Outline each blood parasite and name the species.
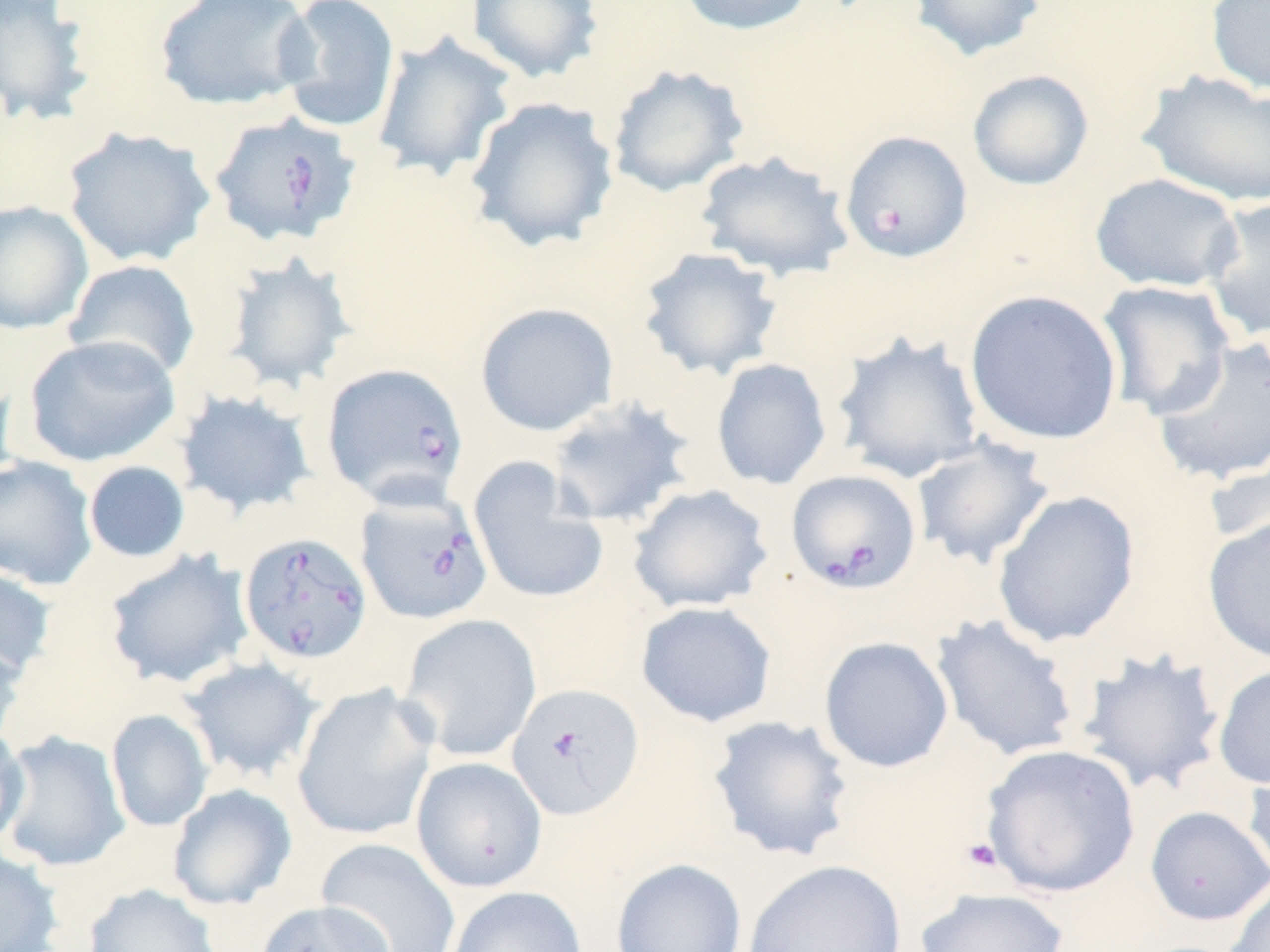
Approximate bounding boxes as (x1, y1, x2, y2) in pixels.
Babesia divergens-infected red blood cells: (206, 111, 362, 248), (321, 362, 469, 508), (785, 468, 922, 594), (355, 489, 493, 625), (238, 531, 373, 664), (506, 683, 644, 821).
No Plasmodium falciparum, Plasmodium ovale, Plasmodium malariae, Plasmodium vivax, or Trypanosoma brucei observed.

Uninfected red blood cell locations: (153, 0, 316, 112), (274, 0, 401, 134), (465, 0, 604, 84), (675, 0, 818, 36), (907, 0, 1047, 62), (1205, 0, 1270, 96), (0, 1, 97, 128), (371, 30, 518, 183), (606, 64, 749, 198), (966, 69, 1094, 191), (1137, 69, 1270, 207), (463, 96, 620, 253), (62, 125, 215, 268), (839, 129, 974, 263), (694, 150, 854, 282), (1089, 172, 1245, 294), (1201, 196, 1270, 342), (0, 200, 94, 334), (636, 247, 784, 381), (221, 252, 357, 395), (64, 259, 201, 380), (1096, 280, 1236, 420), (964, 289, 1124, 447), (475, 302, 618, 436), (831, 331, 986, 483), (22, 334, 180, 467), (1150, 336, 1270, 487), (711, 358, 832, 490), (0, 367, 19, 491), (173, 388, 317, 519), (546, 396, 697, 528), (911, 436, 1055, 570), (1204, 450, 1270, 549), (0, 455, 99, 590), (468, 457, 610, 605), (83, 461, 190, 563), (627, 483, 775, 613), (992, 489, 1141, 648), (1202, 514, 1270, 666), (102, 547, 254, 689), (0, 565, 58, 680), (635, 600, 778, 728), (398, 612, 542, 762), (930, 613, 1082, 763), (0, 634, 28, 751), (819, 636, 954, 773), (1074, 647, 1228, 795), (178, 656, 323, 783), (1212, 661, 1270, 791), (291, 682, 439, 842), (106, 709, 214, 832), (707, 714, 857, 863), (0, 723, 29, 851), (0, 730, 130, 872), (980, 744, 1141, 897), (1242, 755, 1270, 887), (411, 756, 547, 892), (167, 783, 297, 911), (1144, 806, 1270, 927), (316, 837, 462, 952), (0, 848, 64, 952), (611, 858, 746, 952), (742, 859, 907, 952), (1221, 879, 1270, 952), (83, 884, 223, 952), (446, 886, 588, 952), (913, 887, 1071, 952), (255, 899, 396, 952). Platelet locations: (871, 205, 905, 234), (960, 836, 1004, 874). Slide-level diagnosis: Babesia divergens. Single field of view. Thin blood smear. Captured at 1000x magnification. Image is 1270×952 pixels. Light microscopy. May-Grünwald-Giemsa-stained preparation.